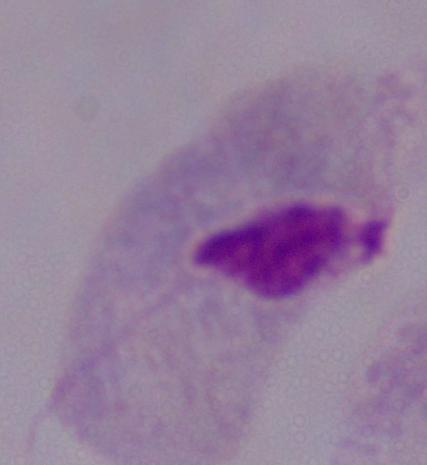 A trichomonad is seen. Captured at 1000x magnification. Photomicrograph.